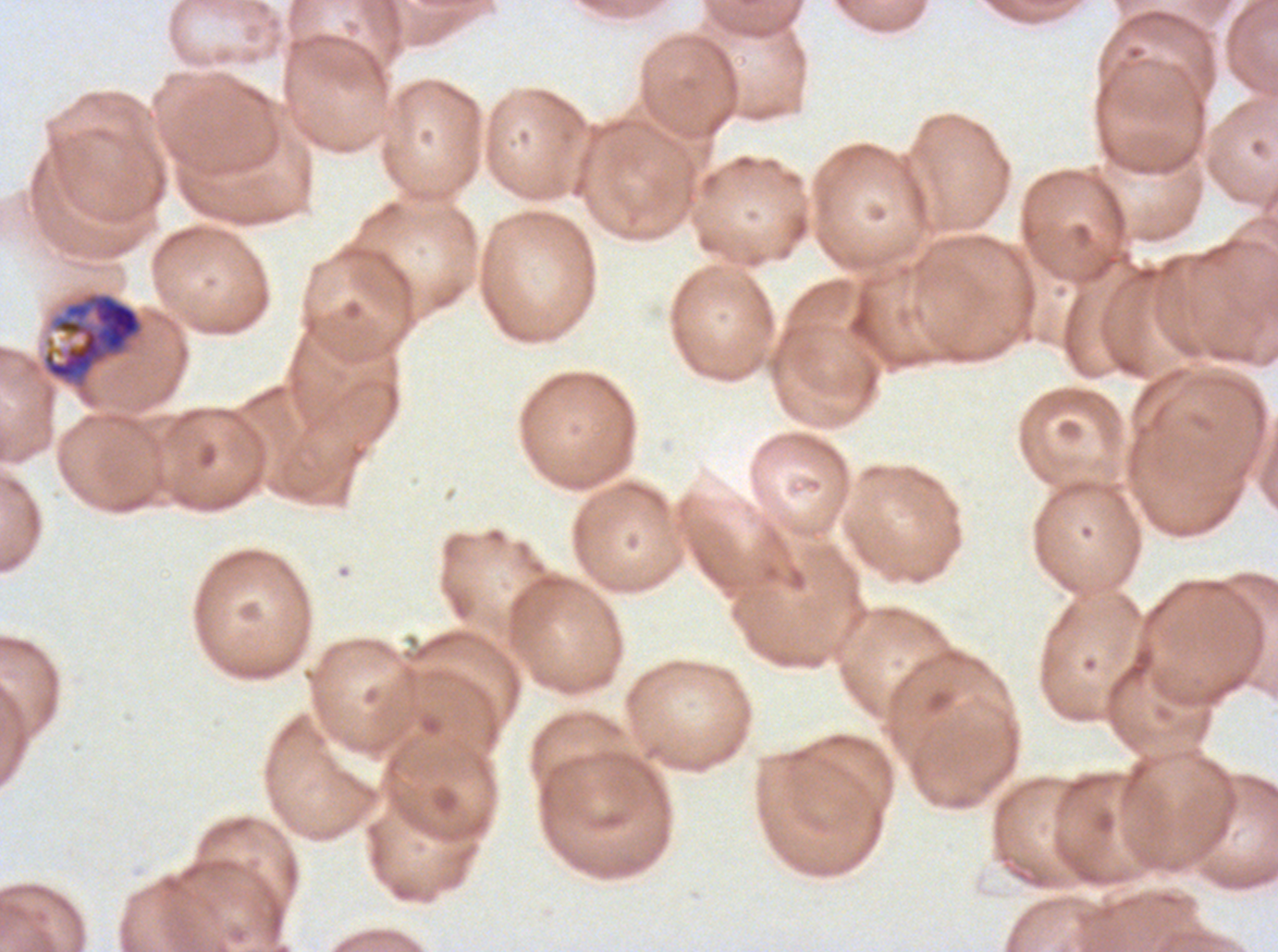
{
  "image_size": "1278×952 pixels",
  "preparation": "thin blood film",
  "field_of_view": "one sub-image of a larger composite",
  "specimen": "ex-vivo Plasmodium falciparum culture from a patient in The Gambia, grown for 24 to 48 hours",
  "late_schizont_locations": "approximate bounding boxes as (x1, y1, x2, y2) in pixels: (43, 293, 142, 381)",
  "stain": "Giemsa"
}